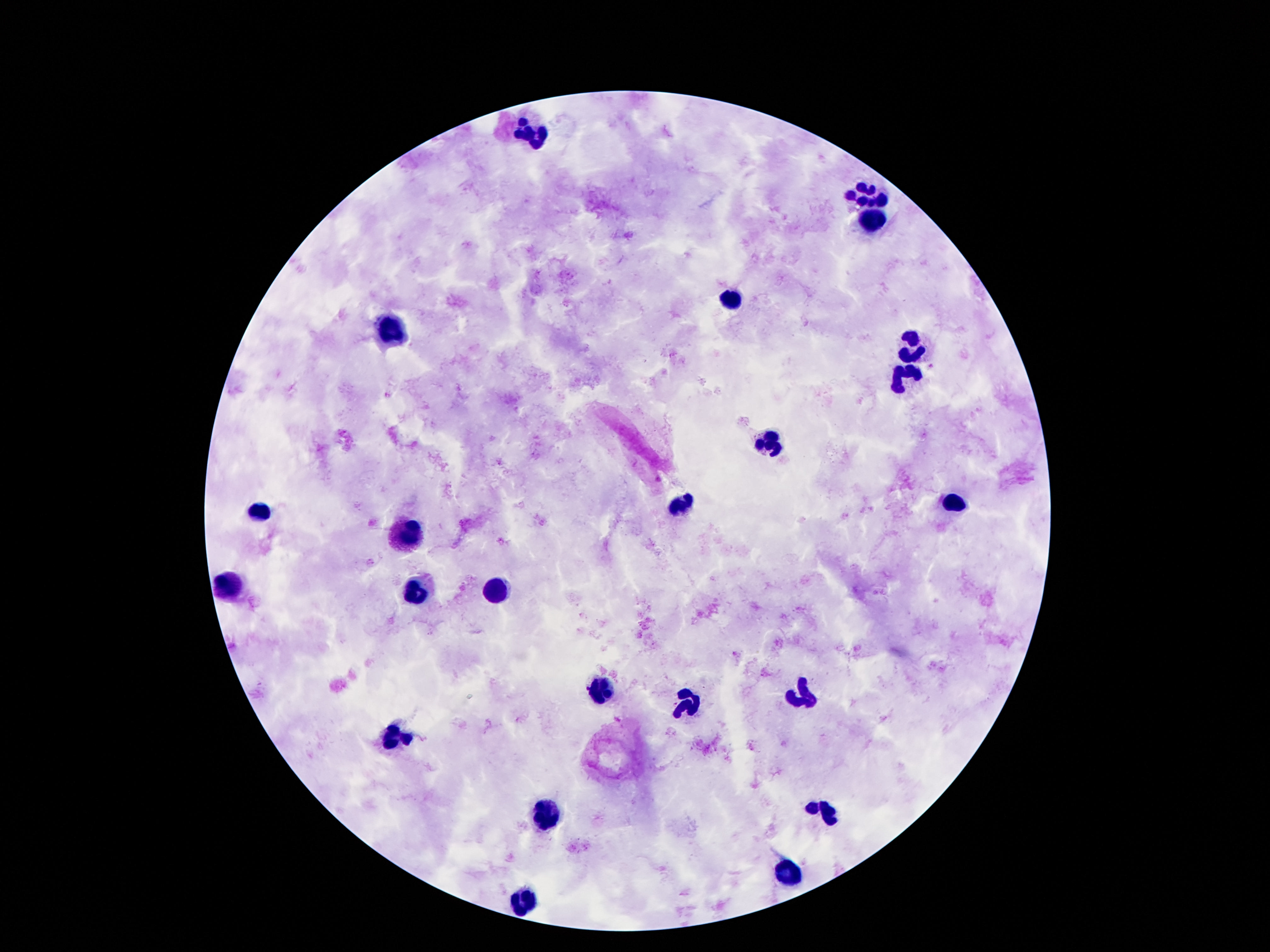
stain = Giemsa
magnification = 100x
preparation = thick blood film
patient malaria status = not infected
image size = 1270×952 pixels
capture = smartphone camera through the microscope eyepiece
field of view = single
leukocyte locations = approximate centers as (x, y) in pixels: (528, 134), (866, 195), (869, 222), (728, 299), (392, 332), (914, 344), (903, 379), (769, 445), (955, 503), (683, 508), (256, 513), (405, 538), (233, 586), (496, 592), (414, 596), (597, 689), (804, 699), (397, 735), (823, 810), (547, 812), (787, 873), (526, 903)